Assess this cell for malaria.
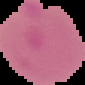
Parasitized.

From a thin blood film. Image is 85×85 pixels. Segmented cell region on a black background.